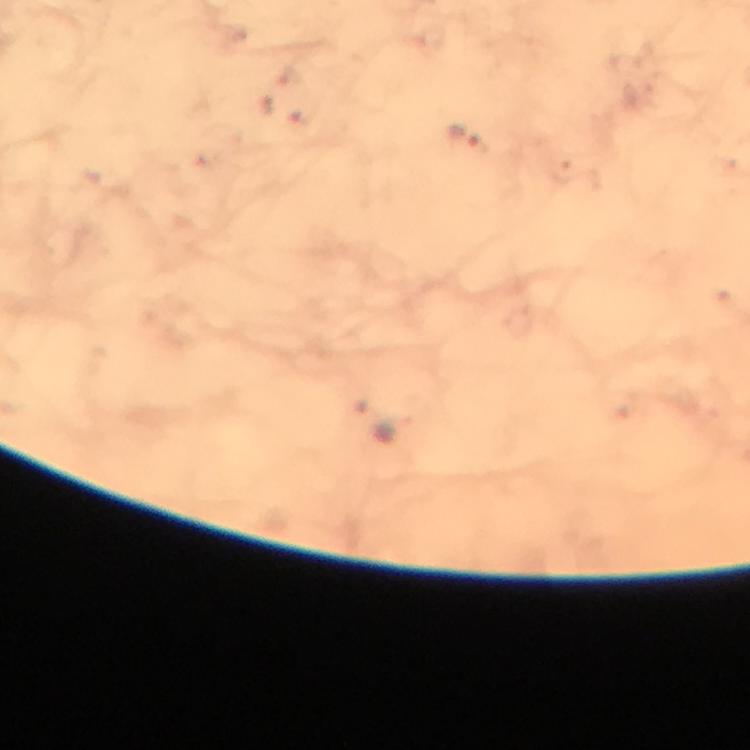
{
  "immersion_oil": "applied",
  "magnification": "100x",
  "stain": "Giemsa",
  "image_size": "750×750 pixels",
  "malaria_parasite_locations": "approximate centers as {x, y} in pixels: {465, 137}",
  "context": "from a diagnostic examination for malaria",
  "capture": "smartphone photograph through a microscope",
  "cropped_from": "a single field of view",
  "preparation": "thick blood smear"
}